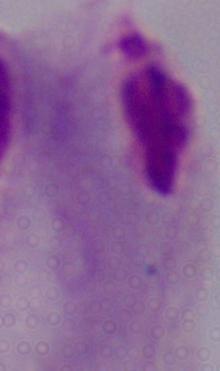

1000x magnification. A trichomonad is seen. Micrograph.